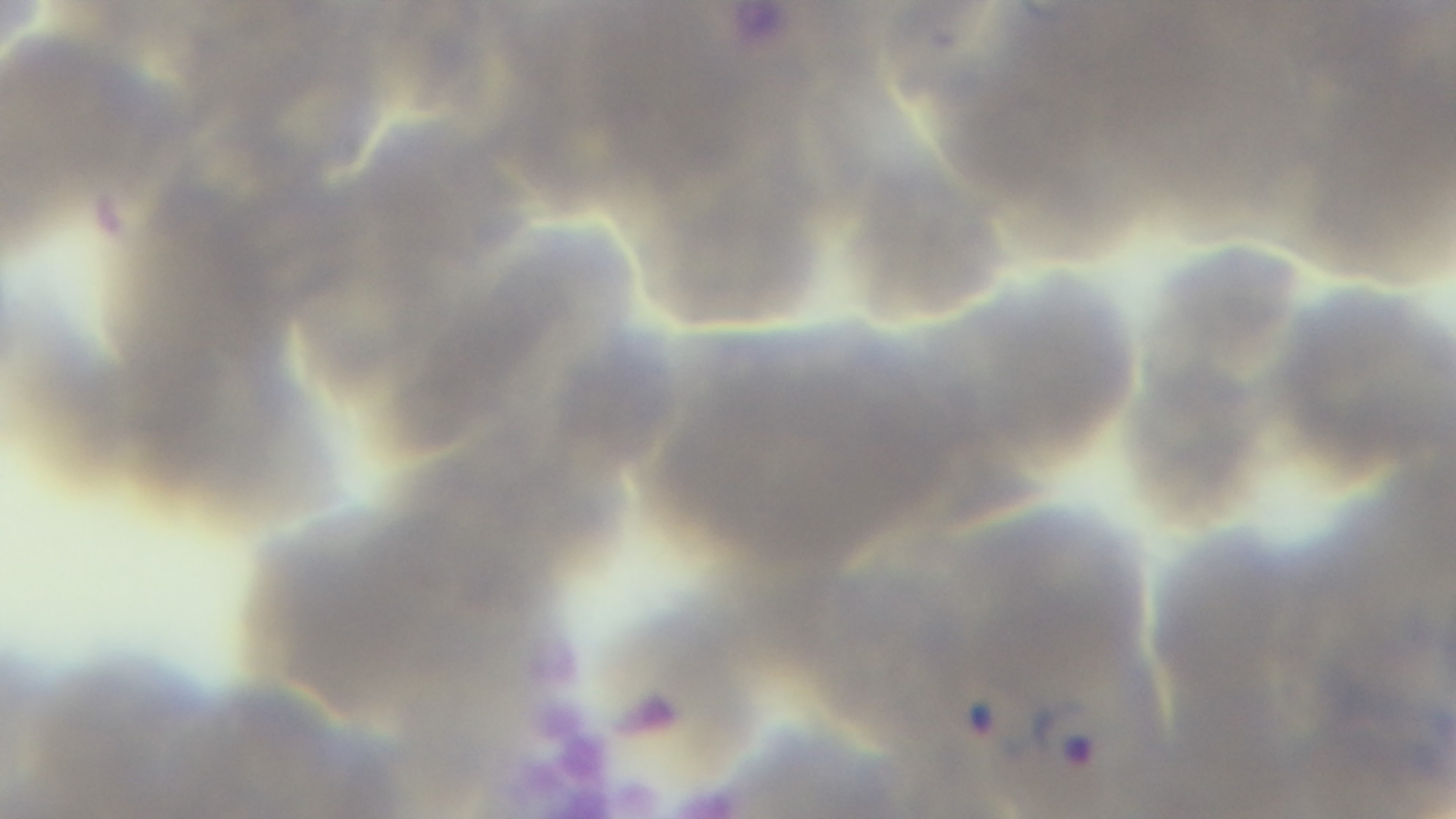
objective = 100x oil immersion
malaria status = positive
modality = light microscopy
field of view = one from the slide
stain = Giemsa
capture = mounted 4K digital camera
preparation = thin